Locate every Plasmodium falciparum-infected red blood cell.
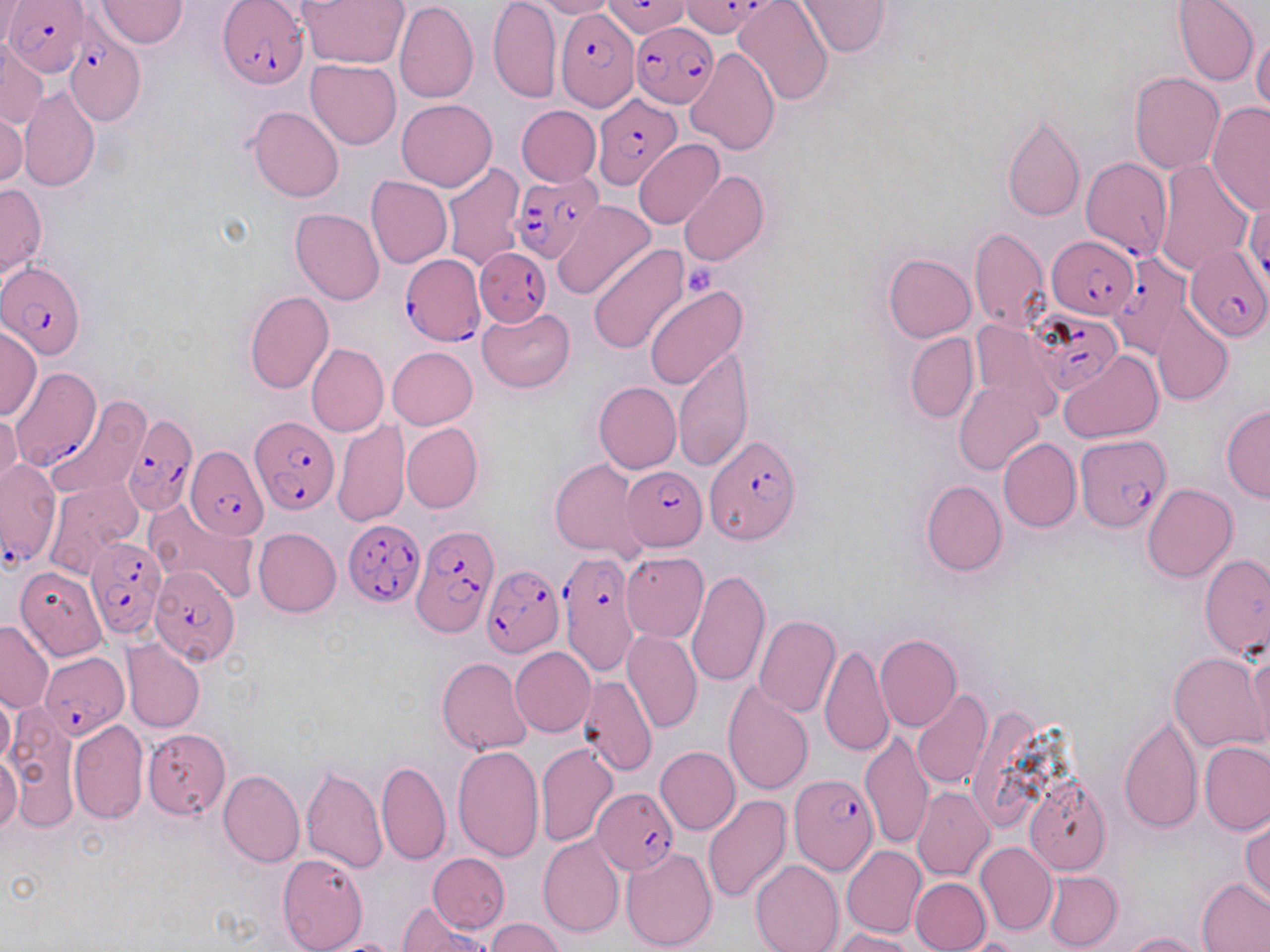
Approximate bounding boxes as named x1/y1/x2/y2 corners in pixels.
Plasmodium falciparum-infected red blood cells (subset): (x1=4, y1=0, x2=88, y2=78), (x1=218, y1=0, x2=307, y2=88), (x1=603, y1=0, x2=690, y2=42), (x1=678, y1=0, x2=772, y2=39), (x1=553, y1=3, x2=639, y2=111), (x1=630, y1=22, x2=719, y2=108), (x1=65, y1=28, x2=145, y2=125), (x1=592, y1=93, x2=681, y2=190), (x1=1081, y1=159, x2=1171, y2=259), (x1=511, y1=171, x2=604, y2=264), (x1=1046, y1=234, x2=1139, y2=318), (x1=1184, y1=245, x2=1267, y2=341), (x1=475, y1=247, x2=551, y2=327), (x1=1110, y1=248, x2=1198, y2=352), (x1=399, y1=255, x2=484, y2=346), (x1=1, y1=261, x2=87, y2=359), (x1=1027, y1=313, x2=1130, y2=397), (x1=10, y1=370, x2=106, y2=478), (x1=123, y1=414, x2=198, y2=515), (x1=250, y1=416, x2=339, y2=514), (x1=1074, y1=434, x2=1170, y2=532), (x1=705, y1=438, x2=801, y2=545), (x1=185, y1=445, x2=270, y2=539), (x1=0, y1=460, x2=61, y2=567), (x1=622, y1=465, x2=708, y2=551), (x1=344, y1=517, x2=425, y2=605), (x1=413, y1=523, x2=497, y2=636), (x1=85, y1=537, x2=167, y2=640), (x1=558, y1=550, x2=639, y2=675), (x1=150, y1=565, x2=241, y2=665), (x1=479, y1=565, x2=563, y2=658), (x1=42, y1=652, x2=126, y2=737), (x1=788, y1=774, x2=878, y2=875), (x1=592, y1=787, x2=679, y2=875).

Uninfected red blood cell locations (subset): (x1=96, y1=0, x2=187, y2=48), (x1=299, y1=0, x2=410, y2=69), (x1=488, y1=0, x2=561, y2=101), (x1=530, y1=0, x2=615, y2=18), (x1=734, y1=0, x2=834, y2=105), (x1=796, y1=0, x2=891, y2=57), (x1=1173, y1=0, x2=1260, y2=87), (x1=0, y1=1, x2=22, y2=48), (x1=394, y1=1, x2=477, y2=104), (x1=1251, y1=32, x2=1270, y2=116), (x1=0, y1=42, x2=48, y2=131), (x1=686, y1=47, x2=780, y2=154), (x1=305, y1=58, x2=401, y2=150), (x1=1130, y1=73, x2=1225, y2=173), (x1=19, y1=86, x2=101, y2=192), (x1=396, y1=99, x2=497, y2=191), (x1=1207, y1=105, x2=1270, y2=213), (x1=247, y1=106, x2=344, y2=202), (x1=516, y1=106, x2=600, y2=186), (x1=1, y1=111, x2=27, y2=189), (x1=1001, y1=111, x2=1085, y2=223), (x1=633, y1=138, x2=724, y2=229), (x1=1153, y1=158, x2=1253, y2=275), (x1=440, y1=161, x2=525, y2=273), (x1=678, y1=170, x2=769, y2=267), (x1=366, y1=175, x2=452, y2=268), (x1=0, y1=183, x2=47, y2=276), (x1=552, y1=199, x2=655, y2=301), (x1=1243, y1=201, x2=1270, y2=288), (x1=290, y1=208, x2=384, y2=304), (x1=969, y1=227, x2=1050, y2=332), (x1=588, y1=244, x2=690, y2=353), (x1=884, y1=254, x2=976, y2=342), (x1=644, y1=286, x2=748, y2=390), (x1=244, y1=290, x2=334, y2=393), (x1=1152, y1=304, x2=1233, y2=405), (x1=478, y1=306, x2=575, y2=392), (x1=969, y1=318, x2=1064, y2=419), (x1=0, y1=326, x2=42, y2=421), (x1=906, y1=333, x2=978, y2=422), (x1=306, y1=343, x2=388, y2=438), (x1=674, y1=344, x2=752, y2=472), (x1=386, y1=346, x2=477, y2=429), (x1=1059, y1=350, x2=1164, y2=444), (x1=954, y1=381, x2=1045, y2=475), (x1=593, y1=382, x2=681, y2=473), (x1=45, y1=395, x2=149, y2=502), (x1=1221, y1=405, x2=1270, y2=502), (x1=0, y1=410, x2=21, y2=495), (x1=332, y1=418, x2=409, y2=527), (x1=402, y1=423, x2=482, y2=513), (x1=997, y1=437, x2=1081, y2=533), (x1=550, y1=458, x2=649, y2=563), (x1=44, y1=479, x2=142, y2=579), (x1=920, y1=480, x2=1006, y2=576), (x1=1141, y1=484, x2=1238, y2=583), (x1=254, y1=528, x2=341, y2=618), (x1=620, y1=552, x2=709, y2=643), (x1=1199, y1=554, x2=1269, y2=659), (x1=14, y1=567, x2=106, y2=661), (x1=686, y1=569, x2=769, y2=688), (x1=754, y1=615, x2=841, y2=718), (x1=0, y1=620, x2=53, y2=713), (x1=623, y1=629, x2=702, y2=734), (x1=875, y1=633, x2=962, y2=732), (x1=123, y1=640, x2=205, y2=732), (x1=819, y1=641, x2=894, y2=760), (x1=509, y1=647, x2=596, y2=737), (x1=1244, y1=648, x2=1270, y2=752), (x1=1168, y1=652, x2=1266, y2=753), (x1=436, y1=656, x2=533, y2=756), (x1=577, y1=674, x2=659, y2=777), (x1=722, y1=681, x2=814, y2=796), (x1=0, y1=689, x2=14, y2=769), (x1=911, y1=690, x2=993, y2=790), (x1=4, y1=711, x2=79, y2=831), (x1=1118, y1=714, x2=1202, y2=833), (x1=68, y1=720, x2=147, y2=823), (x1=143, y1=730, x2=231, y2=819), (x1=859, y1=730, x2=933, y2=849), (x1=1199, y1=741, x2=1269, y2=834), (x1=535, y1=742, x2=619, y2=847), (x1=452, y1=744, x2=544, y2=862), (x1=655, y1=746, x2=740, y2=834), (x1=0, y1=753, x2=22, y2=834), (x1=377, y1=759, x2=451, y2=865), (x1=300, y1=763, x2=387, y2=875), (x1=219, y1=771, x2=304, y2=868), (x1=1025, y1=775, x2=1112, y2=875), (x1=912, y1=786, x2=995, y2=881), (x1=703, y1=794, x2=793, y2=904), (x1=1241, y1=816, x2=1269, y2=905), (x1=537, y1=834, x2=625, y2=937), (x1=976, y1=842, x2=1057, y2=934), (x1=622, y1=847, x2=717, y2=951), (x1=842, y1=847, x2=926, y2=938), (x1=277, y1=852, x2=368, y2=951), (x1=427, y1=852, x2=509, y2=933), (x1=751, y1=859, x2=842, y2=952), (x1=1044, y1=870, x2=1122, y2=951), (x1=910, y1=878, x2=990, y2=952), (x1=1196, y1=879, x2=1270, y2=951), (x1=399, y1=905, x2=491, y2=951), (x1=485, y1=918, x2=567, y2=951), (x1=833, y1=928, x2=916, y2=951), (x1=1124, y1=931, x2=1208, y2=952), (x1=957, y1=937, x2=1026, y2=952), (x1=318, y1=939, x2=408, y2=952). Platelet locations: (x1=682, y1=261, x2=722, y2=298). Slide-level diagnosis: Plasmodium falciparum. Optical microscopy. May-Grünwald-Giemsa-stained preparation. 1000x magnification. One field of a larger specimen. Thin blood smear. Image is 1270×952 pixels.